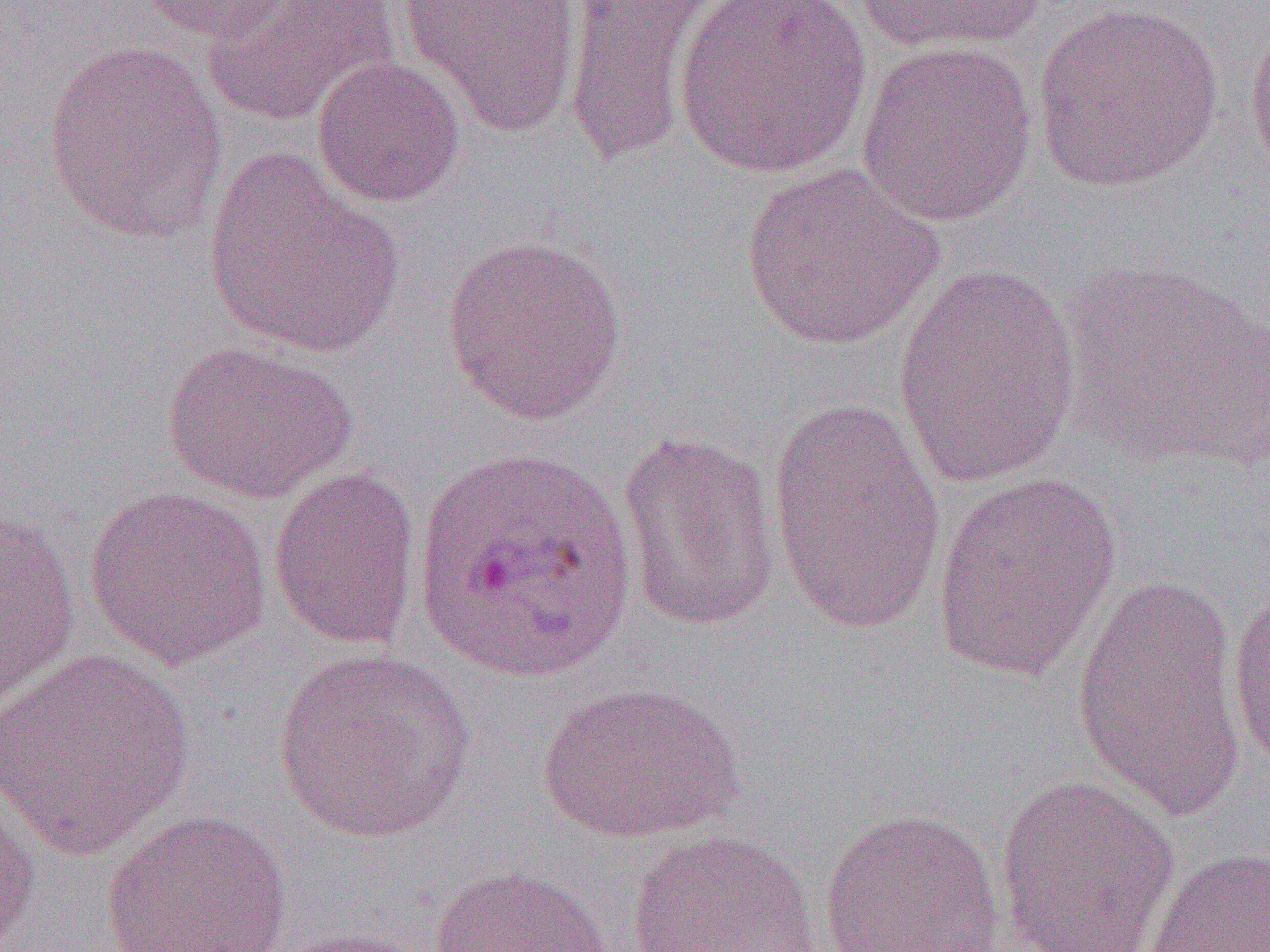
Summary:
  - Coordinate format: approximate bounding boxes as (x1, y1, x2, y2) in pixels
  - Uninfected red blood cell locations: (138, 0, 295, 44), (201, 0, 399, 127), (399, 0, 584, 138), (559, 0, 719, 167), (675, 0, 871, 179), (854, 0, 1051, 56), (1031, 2, 1224, 193), (1244, 11, 1270, 189), (42, 38, 229, 243), (856, 40, 1037, 227), (312, 56, 465, 207), (202, 149, 405, 359), (740, 162, 945, 353), (440, 234, 628, 425), (891, 258, 1085, 489), (1054, 259, 1270, 473), (160, 339, 359, 505), (765, 396, 948, 639), (615, 430, 782, 634), (268, 466, 422, 651), (932, 473, 1122, 682), (83, 485, 273, 671), (1, 509, 81, 714), (1071, 575, 1245, 821), (1226, 579, 1270, 775), (0, 646, 198, 858), (272, 648, 476, 844), (534, 680, 746, 844), (995, 774, 1180, 952), (0, 781, 42, 951), (817, 806, 1006, 952), (101, 809, 293, 952), (623, 828, 822, 952), (1144, 846, 1270, 952), (428, 863, 615, 952), (257, 926, 436, 952)
  - Slide-level diagnosis: Plasmodium ovale
  - Magnification: 1000x
  - Image size: 1270×952 pixels
  - Modality: optical microscopy
  - Field of view: single
  - Preparation: thin blood smear